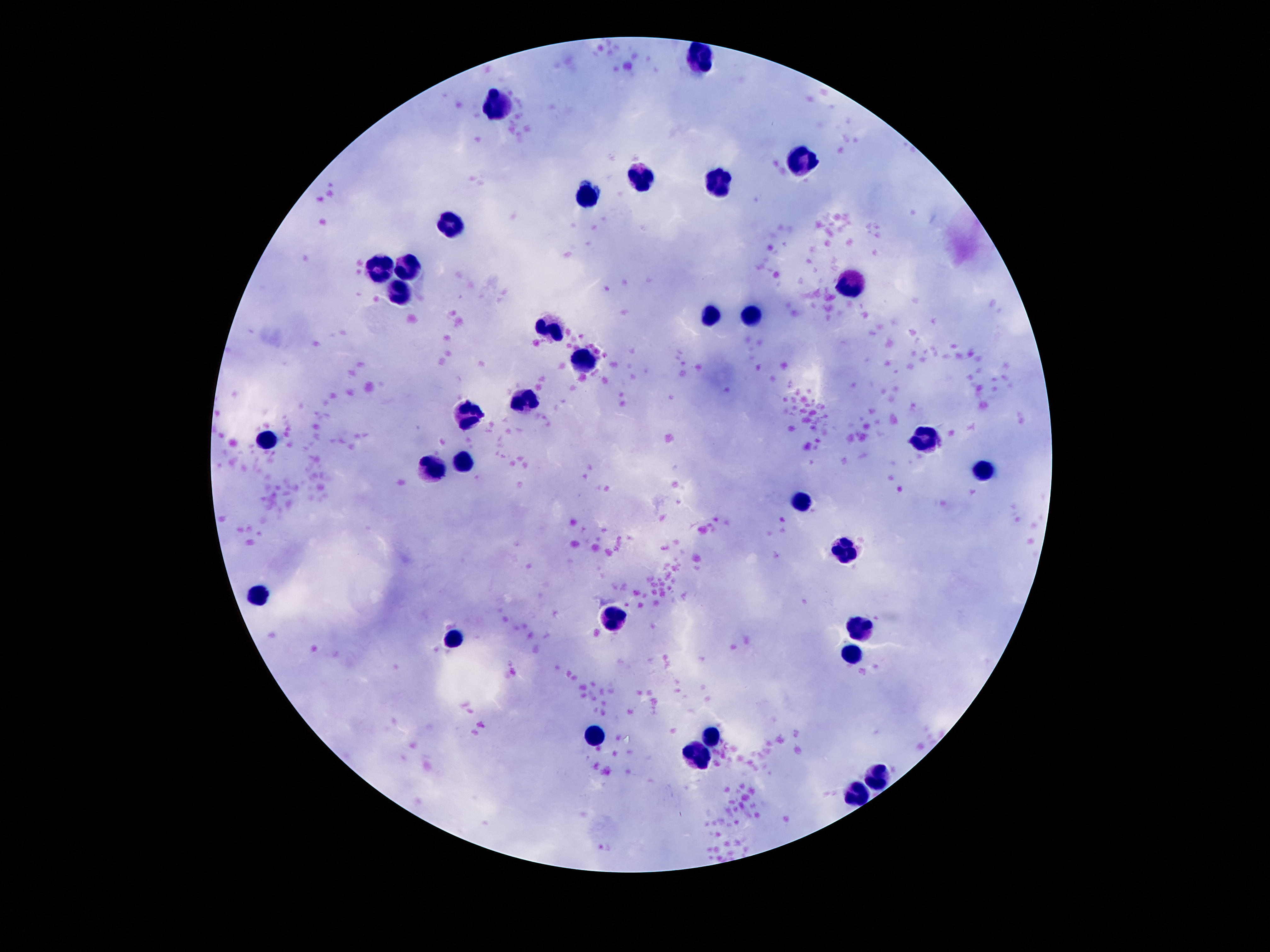

Approximate object centers, in pixels from the top-left corner.
Summary:
  - Leukocyte locations: (x=703, y=58), (x=502, y=107), (x=803, y=161), (x=644, y=176), (x=722, y=186), (x=588, y=197), (x=450, y=223), (x=406, y=266), (x=383, y=270), (x=844, y=284), (x=400, y=289), (x=710, y=317), (x=753, y=318), (x=552, y=329), (x=585, y=357), (x=527, y=400), (x=465, y=416), (x=265, y=441), (x=921, y=441), (x=465, y=459), (x=434, y=470), (x=981, y=470), (x=804, y=501), (x=844, y=551), (x=256, y=596), (x=611, y=618), (x=860, y=628), (x=458, y=644), (x=849, y=655), (x=593, y=735), (x=710, y=737), (x=701, y=753), (x=878, y=773), (x=856, y=792)
  - Stain: Giemsa
  - Patient malaria status: not infected
  - Magnification: 100x
  - Image size: 1270×952 pixels
  - Preparation: thick peripheral-blood smear
  - Field of view: one from this slide
  - Capture: smartphone camera through the microscope eyepiece